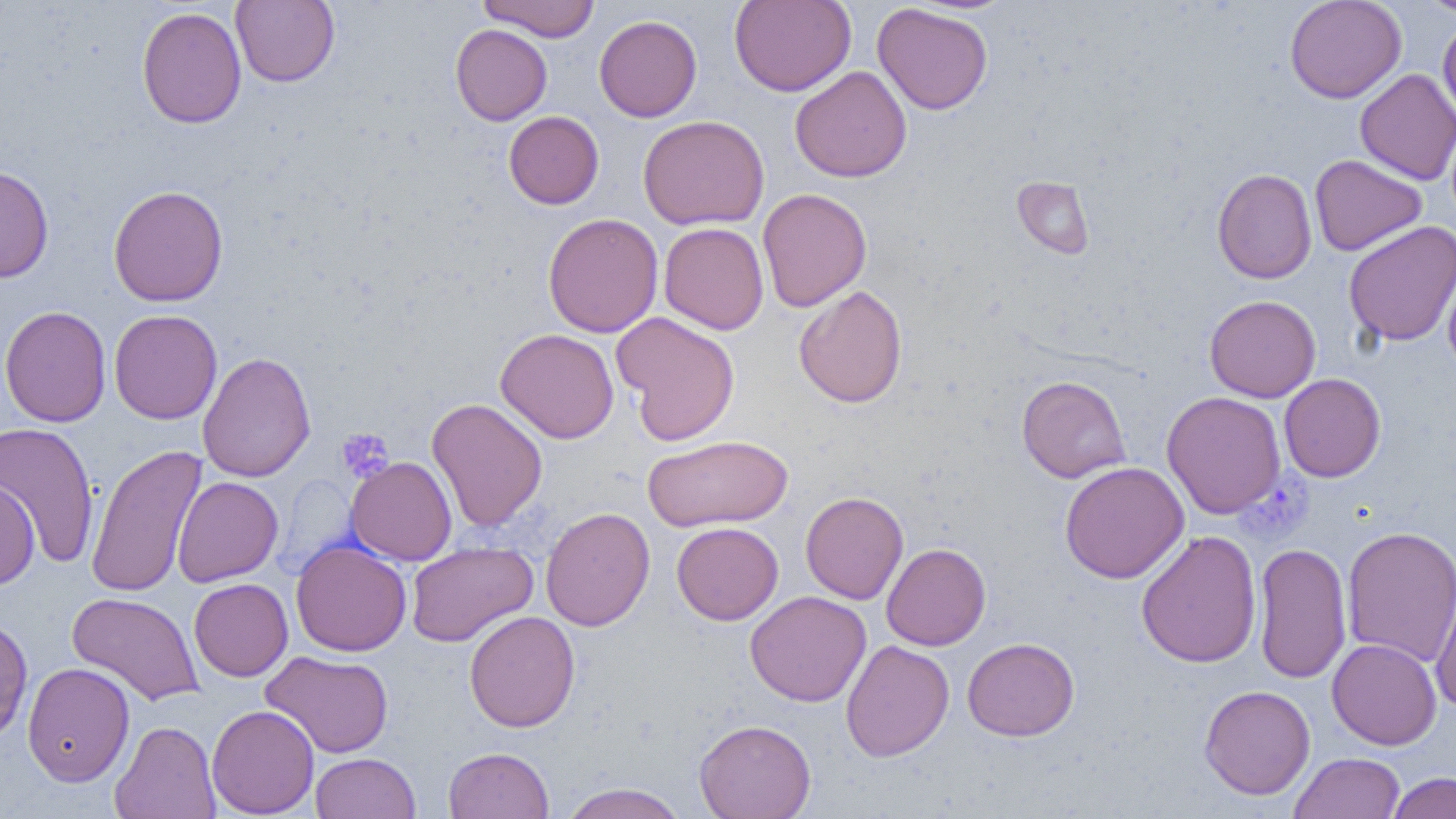
slide-level diagnosis = no evidence of blood parasites
uninfected red blood cell locations = approximate bounding boxes as (x1,y1)-(x2,y2) corner pairs in pixels: (230,0)-(340,87), (478,0)-(601,42), (729,0)-(856,97), (1284,0)-(1406,103), (1419,0)-(1455,17), (872,3)-(993,115), (136,5)-(247,129), (594,15)-(702,122), (1438,19)-(1456,124), (450,24)-(552,125), (790,66)-(912,183), (1355,68)-(1455,186), (504,111)-(604,209), (638,115)-(769,230), (1309,154)-(1426,256), (0,164)-(54,283), (1212,168)-(1317,284), (1012,176)-(1095,258), (108,185)-(228,307), (757,188)-(872,312), (542,213)-(663,338), (1343,220)-(1456,346), (658,222)-(769,334), (1441,256)-(1456,375), (793,284)-(908,408), (1205,295)-(1321,402), (0,305)-(111,427), (109,309)-(222,424), (611,311)-(741,446), (496,328)-(619,443), (197,351)-(316,482), (1279,373)-(1386,482), (1016,374)-(1130,483), (1161,391)-(1287,519), (426,398)-(548,532), (0,421)-(100,569), (642,434)-(793,532), (86,444)-(207,598), (346,456)-(457,565), (1060,461)-(1189,584), (172,476)-(283,586), (0,479)-(40,588), (800,491)-(908,604), (540,506)-(655,631), (671,522)-(784,625), (1341,525)-(1456,668), (1136,529)-(1262,668), (291,539)-(412,657), (406,542)-(537,647), (881,542)-(991,650), (1253,542)-(1352,685), (1430,576)-(1455,713), (189,578)-(293,682), (744,590)-(872,707), (67,592)-(204,706), (464,610)-(580,733), (0,615)-(33,742), (962,637)-(1080,741), (1327,638)-(1442,750), (840,640)-(954,762), (260,650)-(393,758), (22,662)-(135,787), (1199,684)-(1315,800), (206,704)-(319,818), (694,719)-(816,818), (110,720)-(221,819), (443,746)-(554,819), (310,752)-(421,819), (1289,752)-(1405,819), (1387,772)-(1455,818), (558,782)-(690,819)
preparation = thin blood film
modality = optical microscopy
magnification = 1000x
image size = 1456×819 pixels
field of view = one of a larger specimen
platelet locations = approximate bounding boxes as (x1,y1)-(x2,y2) corner pairs in pixels: (336,428)-(394,482)